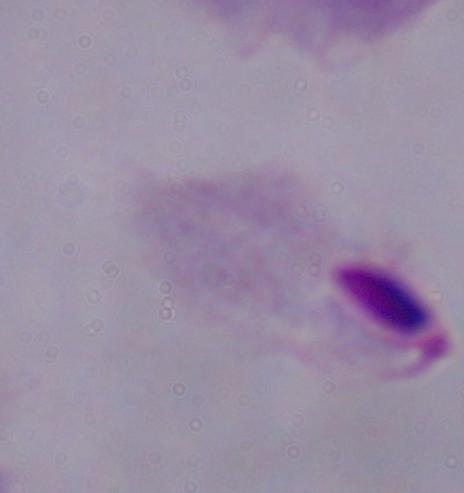

1000x magnification. A trichomonad is seen. Photomicrograph.